Give the position of every Plasmodium parasite and every leukocyte.
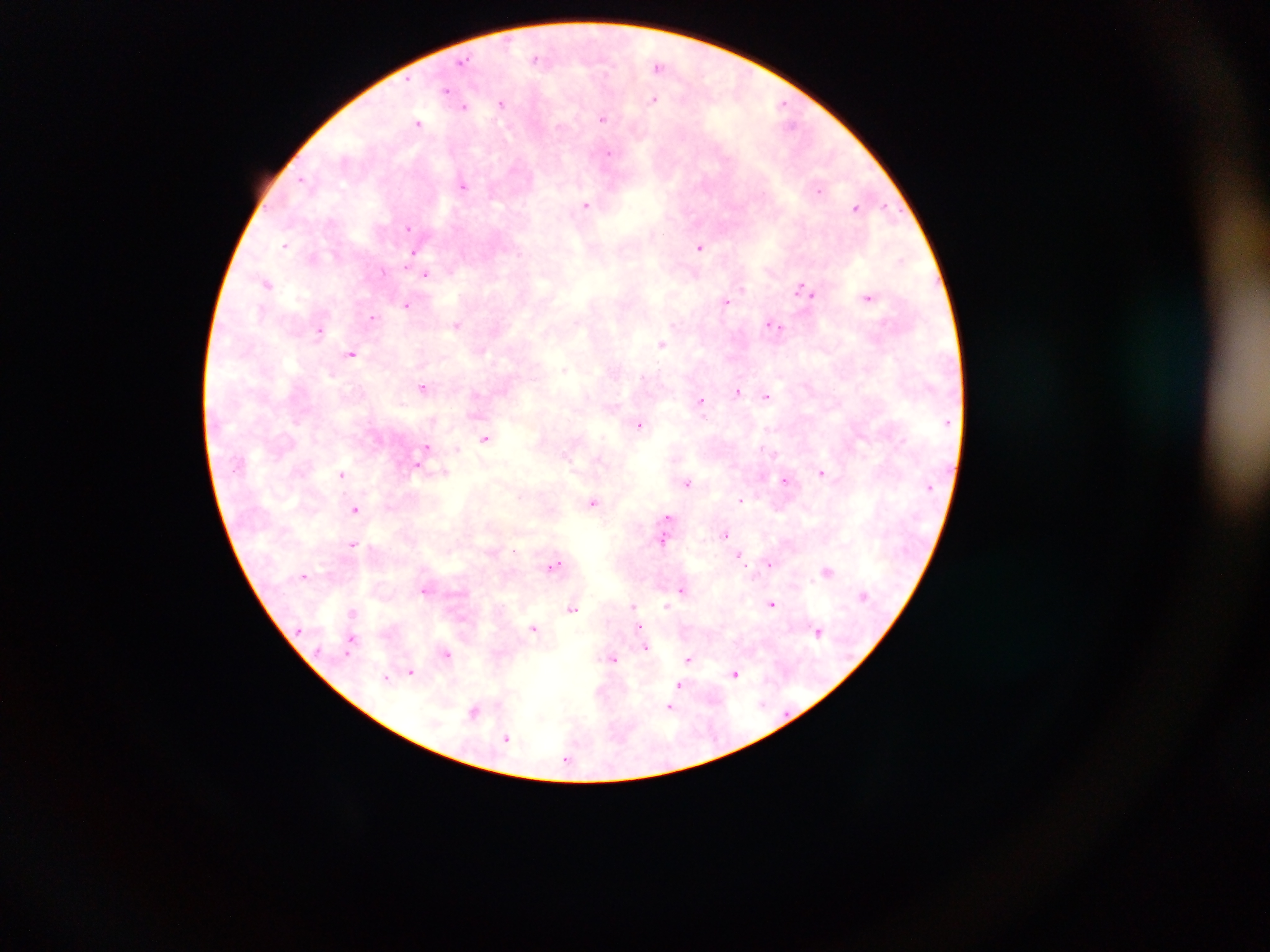
Approximate centers as {x, y} in pixels.
Plasmodium parasites: {538, 58}, {462, 62}, {658, 65}, {446, 90}, {655, 98}, {502, 103}, {784, 105}, {464, 106}, {603, 117}, {419, 122}, {607, 153}, {463, 183}, {819, 189}, {587, 205}, {885, 205}, {856, 206}, {408, 227}, {285, 244}, {701, 246}, {415, 253}, {427, 274}, {267, 283}, {807, 290}, {869, 296}, {725, 301}, {408, 304}, {373, 318}, {458, 325}, {773, 325}, {321, 330}, {663, 343}, {353, 353}, {425, 387}, {737, 392}, {767, 396}, {701, 402}, {639, 423}, {487, 437}, {427, 448}, {424, 454}, {417, 464}, {822, 472}, {342, 475}, {785, 480}, {687, 482}, {741, 499}, {594, 502}, {355, 509}, {669, 517}, {668, 525}, {725, 534}, {664, 539}, {354, 543}, {740, 554}, {769, 562}, {555, 563}, {828, 571}, {306, 575}, {425, 589}, {683, 590}, {772, 603}, {634, 605}, {572, 607}, {666, 607}, {354, 612}, {640, 626}, {535, 628}, {818, 631}, {353, 636}, {646, 647}, {447, 653}, {614, 658}, {689, 659}, {411, 671}, {736, 672}, {386, 677}, {681, 685}, {671, 706}, {474, 711}, {506, 738}, {568, 757}.
No leukocytes observed.

country = Ghana
field of view = single
capture = mobile-phone photograph through a microscope
preparation = thick blood film
image size = 1270×952 pixels